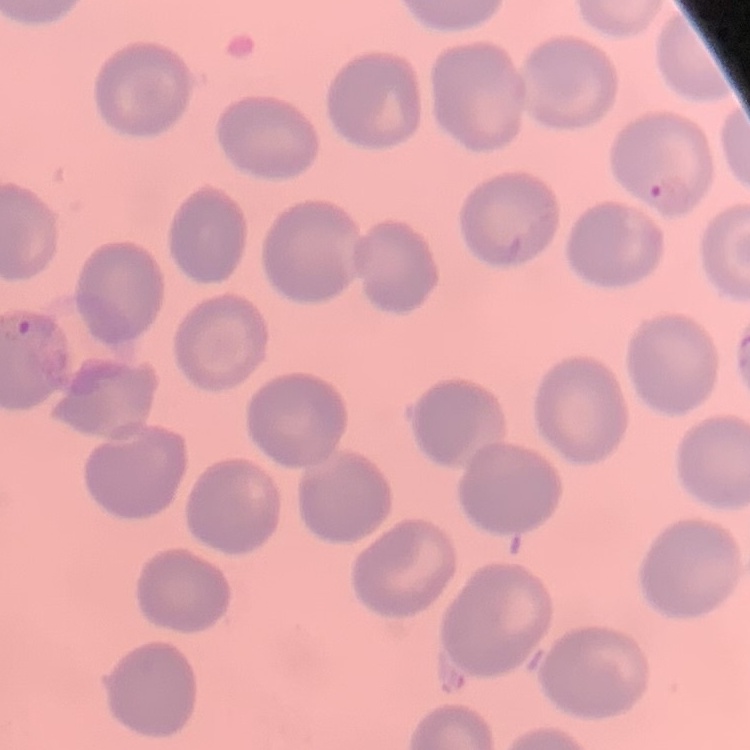 The red blood cells show no rouleaux formation. One tile cut from a larger photomicrograph. Stained with either Field's or Giemsa. Thin peripheral smear.